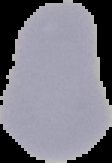
Image is 112×163 pixels. From a thin blood smear. Result: no Plasmodium parasites detected. Segmented cell region on a black background.